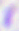
400x magnification. Toxoplasma gondii is shown. Micrograph.